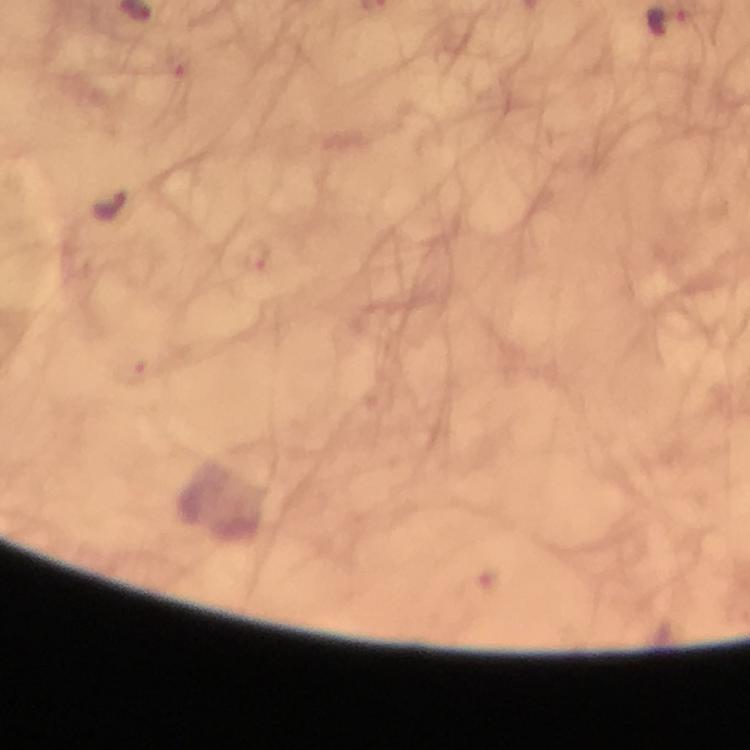

Approximate centers as (x, y) in pixels.
Summary:
  - Plasmodium parasite locations: (255, 256), (132, 370)
  - Stain: Giemsa
  - Context: from a malaria diagnostic workup
  - Preparation: thick blood film
  - Capture: smartphone photograph through a microscope
  - Magnification: 100x
  - Image size: 750×750 pixels
  - Cropped from: one field of view
  - Immersion oil: applied